Report the malaria status of this cell.
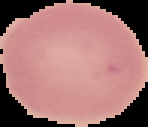

It is uninfected.

From a thin blood film. Segmented cell region on a black background. Image is 148×127 pixels.